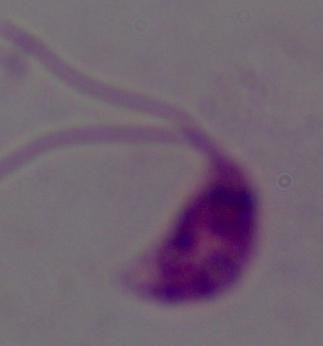 Photomicrograph. 1000x magnification. A Leishmania parasite is shown.